Identify the parasite.
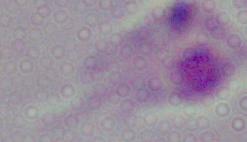

This is Leishmania.

Summary:
  - Modality: photomicrograph
  - Magnification: 1000x